Outline each Plasmodium falciparum parasite and classify it by life-cycle stage.
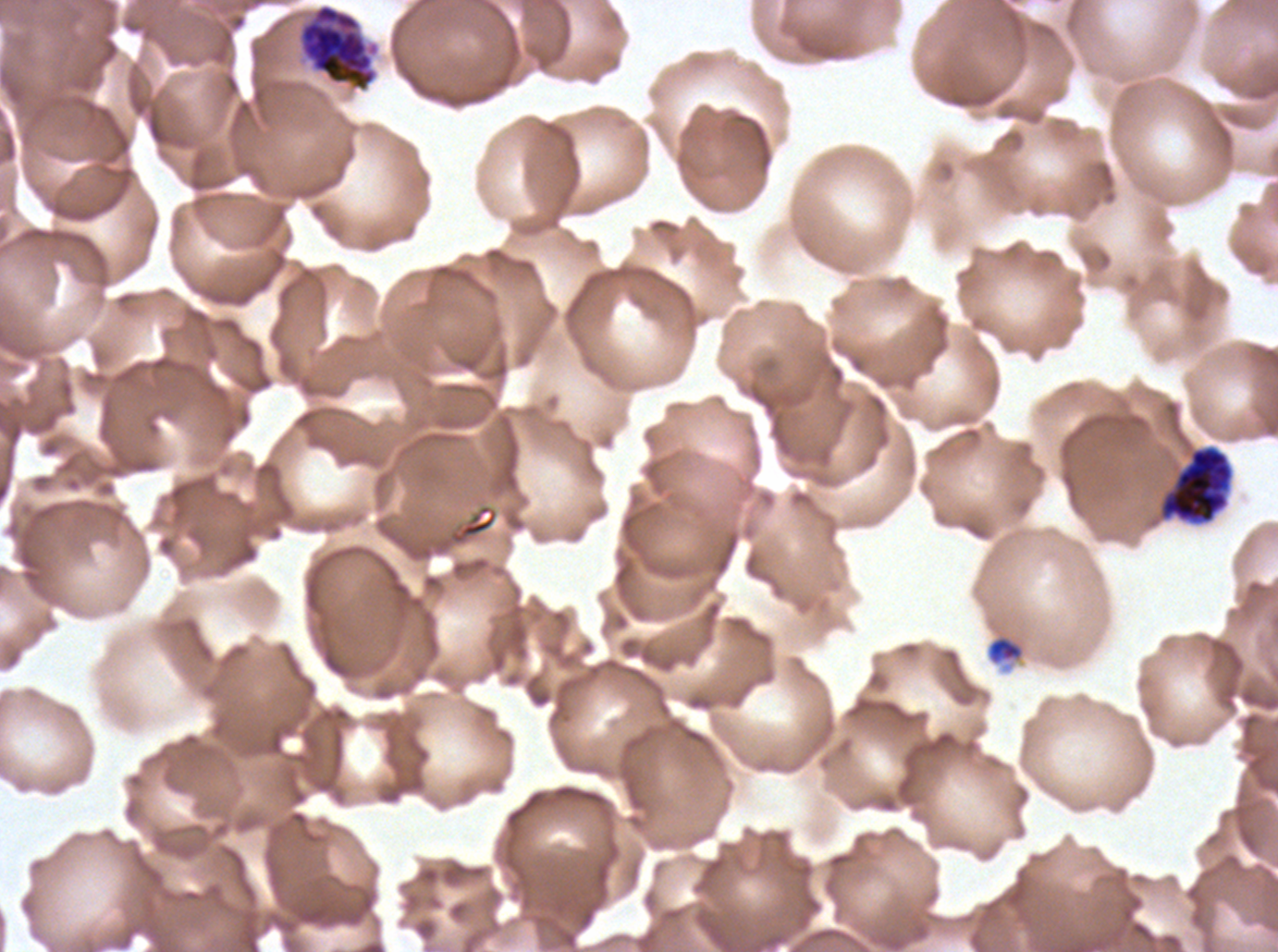

Approximate bounding boxes as {x1, y1, x2, y2} in pixels.
Late schizonts: {298, 3, 379, 92}, {1161, 445, 1233, 523}.
No rings, late-ring/early-trophozoite forms, mid trophozoites, late trophozoites, early schizonts, segmenters, or gametocytes observed.

Debris locations: {986, 634, 1026, 666}. A sub-image separated from a larger composite. Thin blood smear. Plasmodium falciparum cultured ex vivo for 24 to 48 hours, from a patient in The Gambia. Image is 1278×952 pixels. Giemsa-stained preparation.